State the blood parasite species.
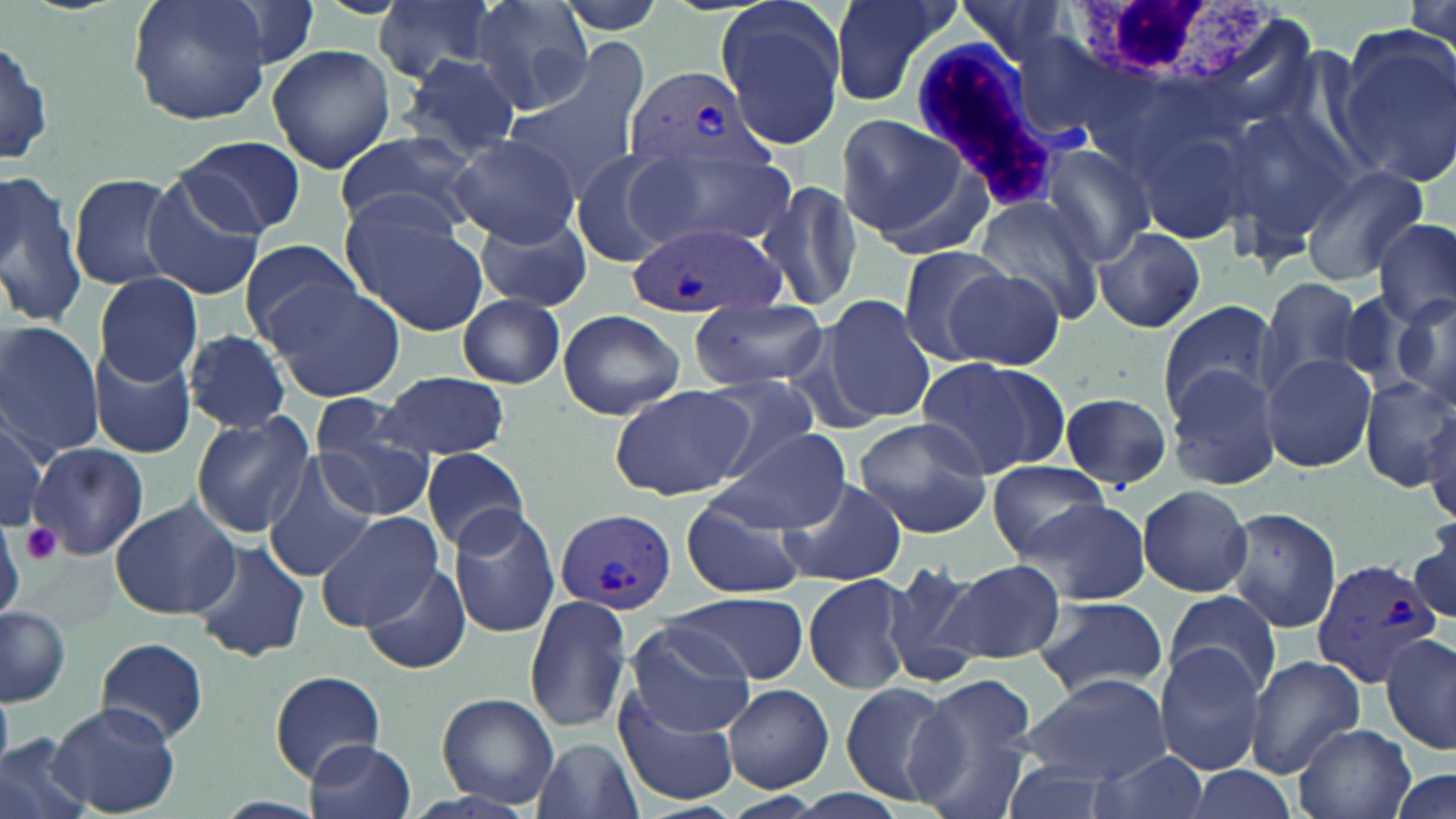

Plasmodium vivax.

Approximate bounding boxes as named x1/y1/x2/y2 corners in pixels. White blood cell locations: (x1=1073, y1=0, x2=1286, y2=86), (x1=912, y1=37, x2=1092, y2=202). Platelet locations: (x1=21, y1=521, x2=63, y2=566). Uninfected red blood cell locations: (x1=128, y1=0, x2=270, y2=125), (x1=470, y1=0, x2=594, y2=115), (x1=552, y1=0, x2=670, y2=35), (x1=715, y1=0, x2=847, y2=149), (x1=827, y1=0, x2=960, y2=110), (x1=950, y1=0, x2=1074, y2=70), (x1=374, y1=1, x2=498, y2=81), (x1=1335, y1=30, x2=1455, y2=189), (x1=0, y1=32, x2=53, y2=172), (x1=505, y1=43, x2=652, y2=192), (x1=267, y1=44, x2=396, y2=175), (x1=399, y1=52, x2=523, y2=164), (x1=1220, y1=108, x2=1354, y2=261), (x1=835, y1=111, x2=977, y2=252), (x1=1127, y1=118, x2=1252, y2=246), (x1=333, y1=129, x2=481, y2=237), (x1=450, y1=134, x2=581, y2=245), (x1=179, y1=135, x2=304, y2=237), (x1=1037, y1=142, x2=1154, y2=266), (x1=571, y1=149, x2=680, y2=268), (x1=632, y1=150, x2=795, y2=254), (x1=1300, y1=163, x2=1429, y2=282), (x1=0, y1=170, x2=87, y2=328), (x1=68, y1=171, x2=182, y2=290), (x1=138, y1=171, x2=265, y2=301), (x1=755, y1=176, x2=867, y2=316), (x1=974, y1=194, x2=1107, y2=325), (x1=336, y1=199, x2=488, y2=337), (x1=478, y1=212, x2=593, y2=314), (x1=1374, y1=218, x2=1455, y2=330), (x1=1094, y1=227, x2=1205, y2=332), (x1=237, y1=238, x2=362, y2=349), (x1=897, y1=245, x2=1016, y2=363), (x1=942, y1=265, x2=1066, y2=370), (x1=94, y1=273, x2=203, y2=386), (x1=1259, y1=276, x2=1364, y2=390), (x1=264, y1=280, x2=408, y2=403), (x1=1390, y1=293, x2=1456, y2=413), (x1=458, y1=294, x2=566, y2=387), (x1=822, y1=295, x2=939, y2=425), (x1=689, y1=298, x2=828, y2=392), (x1=1157, y1=299, x2=1277, y2=417), (x1=557, y1=308, x2=685, y2=420), (x1=0, y1=323, x2=104, y2=457), (x1=183, y1=330, x2=293, y2=433), (x1=88, y1=346, x2=195, y2=457), (x1=1261, y1=354, x2=1378, y2=472), (x1=914, y1=355, x2=1069, y2=480), (x1=1166, y1=364, x2=1282, y2=492), (x1=375, y1=372, x2=512, y2=459), (x1=693, y1=374, x2=824, y2=480), (x1=1359, y1=376, x2=1456, y2=492), (x1=609, y1=385, x2=751, y2=502), (x1=1059, y1=392, x2=1172, y2=491), (x1=309, y1=402, x2=436, y2=519), (x1=0, y1=410, x2=50, y2=534), (x1=1426, y1=412, x2=1456, y2=527), (x1=189, y1=413, x2=314, y2=537), (x1=851, y1=417, x2=995, y2=537), (x1=717, y1=429, x2=851, y2=535), (x1=29, y1=442, x2=147, y2=561), (x1=421, y1=446, x2=530, y2=552), (x1=263, y1=454, x2=376, y2=583), (x1=989, y1=459, x2=1107, y2=558), (x1=776, y1=477, x2=909, y2=587), (x1=1137, y1=484, x2=1252, y2=597), (x1=679, y1=495, x2=809, y2=600), (x1=109, y1=497, x2=240, y2=621), (x1=1024, y1=502, x2=1150, y2=603), (x1=1220, y1=505, x2=1343, y2=633), (x1=447, y1=506, x2=560, y2=638), (x1=315, y1=512, x2=443, y2=628), (x1=1412, y1=521, x2=1456, y2=627), (x1=0, y1=524, x2=25, y2=617), (x1=190, y1=539, x2=309, y2=662), (x1=878, y1=560, x2=990, y2=689), (x1=939, y1=560, x2=1066, y2=665), (x1=359, y1=561, x2=469, y2=675), (x1=802, y1=573, x2=916, y2=694), (x1=1165, y1=589, x2=1281, y2=699), (x1=667, y1=592, x2=807, y2=683), (x1=1031, y1=595, x2=1169, y2=702), (x1=523, y1=596, x2=634, y2=734), (x1=0, y1=607, x2=70, y2=705), (x1=626, y1=621, x2=756, y2=736), (x1=1381, y1=634, x2=1456, y2=755), (x1=95, y1=636, x2=208, y2=744), (x1=1154, y1=645, x2=1267, y2=774), (x1=1243, y1=656, x2=1366, y2=778), (x1=270, y1=669, x2=383, y2=780), (x1=1022, y1=671, x2=1171, y2=785), (x1=838, y1=680, x2=958, y2=806), (x1=909, y1=680, x2=1036, y2=817), (x1=723, y1=684, x2=834, y2=791), (x1=614, y1=688, x2=740, y2=808), (x1=0, y1=690, x2=13, y2=768), (x1=437, y1=693, x2=560, y2=807), (x1=50, y1=704, x2=182, y2=816), (x1=1293, y1=724, x2=1415, y2=819), (x1=0, y1=735, x2=91, y2=819), (x1=530, y1=735, x2=643, y2=819), (x1=307, y1=737, x2=418, y2=819), (x1=1086, y1=752, x2=1212, y2=819), (x1=996, y1=755, x2=1123, y2=819), (x1=1178, y1=764, x2=1301, y2=819), (x1=1391, y1=770, x2=1455, y2=819), (x1=724, y1=792, x2=820, y2=817). Plasmodium vivax-infected red blood cell locations: (x1=623, y1=67, x2=773, y2=176), (x1=627, y1=224, x2=783, y2=315), (x1=555, y1=509, x2=678, y2=614), (x1=1308, y1=554, x2=1445, y2=690). Thin blood smear. May-Grünwald-Giemsa stain. Single field of view. Optical microscopy. Captured at 1000x magnification. Image is 1456×819 pixels.